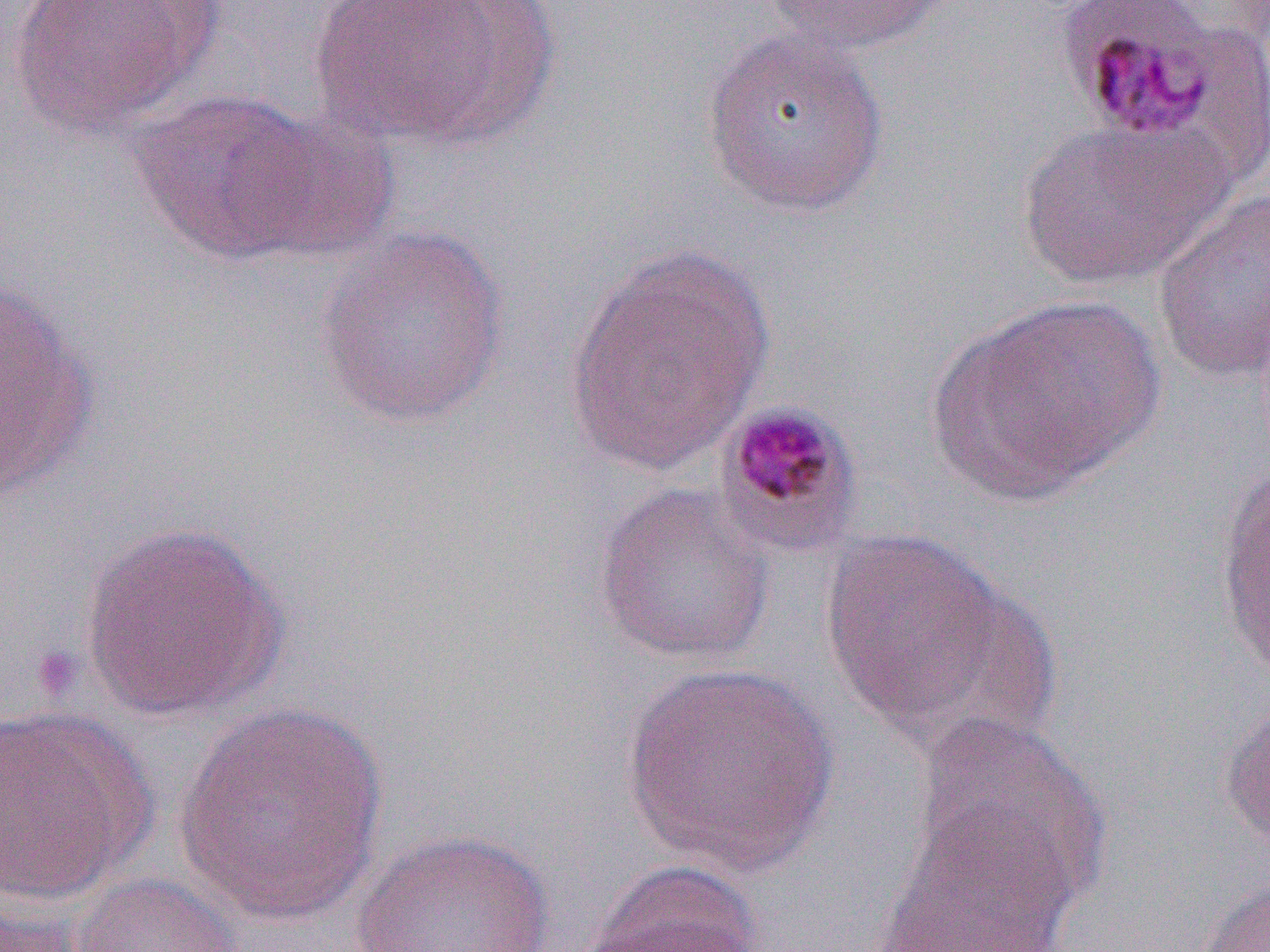

slide-level diagnosis = Plasmodium malariae
uninfected red blood cell locations = approximate bounding boxes as named x1/y1/x2/y2 corners in pixels: (x1=7, y1=0, x2=214, y2=140), (x1=308, y1=0, x2=533, y2=148), (x1=764, y1=0, x2=955, y2=57), (x1=699, y1=26, x2=890, y2=218), (x1=128, y1=88, x2=325, y2=263), (x1=236, y1=110, x2=400, y2=265), (x1=1016, y1=117, x2=1231, y2=290), (x1=1152, y1=185, x2=1270, y2=386), (x1=313, y1=224, x2=511, y2=428), (x1=561, y1=245, x2=779, y2=478), (x1=0, y1=278, x2=100, y2=504), (x1=929, y1=293, x2=1166, y2=505), (x1=1214, y1=454, x2=1270, y2=688), (x1=592, y1=480, x2=776, y2=668), (x1=78, y1=522, x2=290, y2=722), (x1=818, y1=527, x2=1037, y2=746), (x1=621, y1=660, x2=840, y2=876), (x1=1219, y1=696, x2=1270, y2=854), (x1=171, y1=702, x2=388, y2=924), (x1=0, y1=705, x2=157, y2=903), (x1=910, y1=712, x2=1109, y2=908), (x1=873, y1=804, x2=1082, y2=952), (x1=348, y1=829, x2=557, y2=951), (x1=579, y1=860, x2=766, y2=951), (x1=69, y1=872, x2=247, y2=952), (x1=1192, y1=879, x2=1270, y2=952), (x1=0, y1=899, x2=92, y2=952)
image size = 1270×952 pixels
magnification = 1000x
modality = light microscopy
Plasmodium malariae-infected red blood cell locations = approximate bounding boxes as named x1/y1/x2/y2 corners in pixels: (x1=1050, y1=1, x2=1242, y2=151), (x1=713, y1=398, x2=867, y2=559)
preparation = thin blood smear
field of view = single
platelet locations = approximate bounding boxes as named x1/y1/x2/y2 corners in pixels: (x1=27, y1=643, x2=86, y2=704)